Identify the parasite.
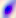
This is Toxoplasma gondii.

Summary:
  - Magnification: 400x
  - Modality: photomicrograph